Name the parasite shown.
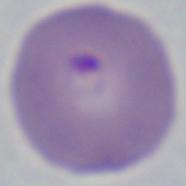
Babesia.

modality = micrograph
magnification = 1000x